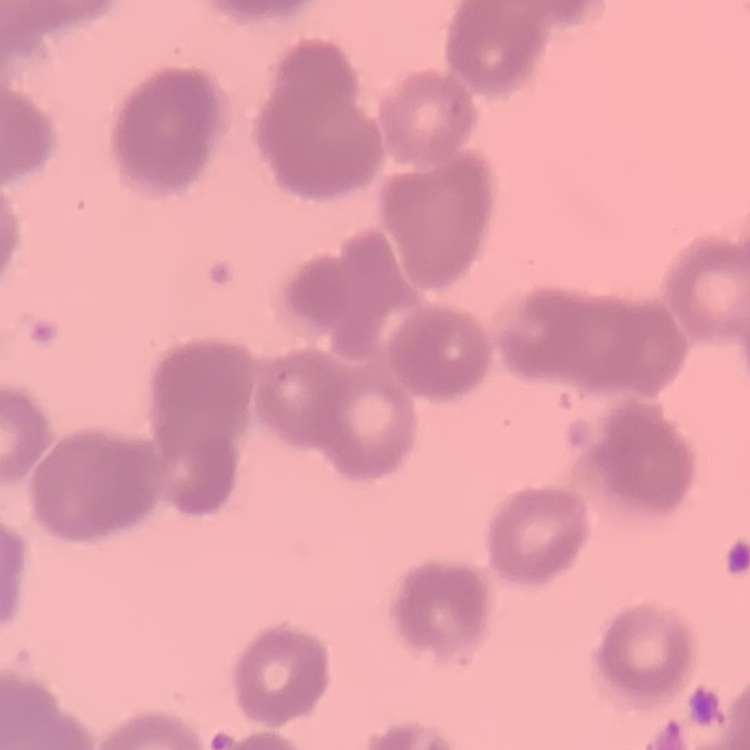
The red blood cells show rouleaux formation. Square crop of a larger photomicrograph. Thin blood smear. Field's or Giemsa stain.